Identify the cell.
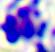

This is a leukocyte.

{
  "magnification": "400x",
  "modality": "micrograph"
}